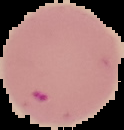
image size = 124×130 pixels
preparation = thin blood smear
result = Plasmodium parasites identified
image type = segmented cell region on a black background